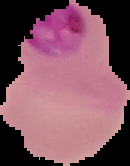

Summary:
  - Malaria status: parasitized
  - Preparation: thin blood smear
  - Image type: cell region segmented out of the field of view; surrounding area masked to black
  - Image size: 130×166 pixels